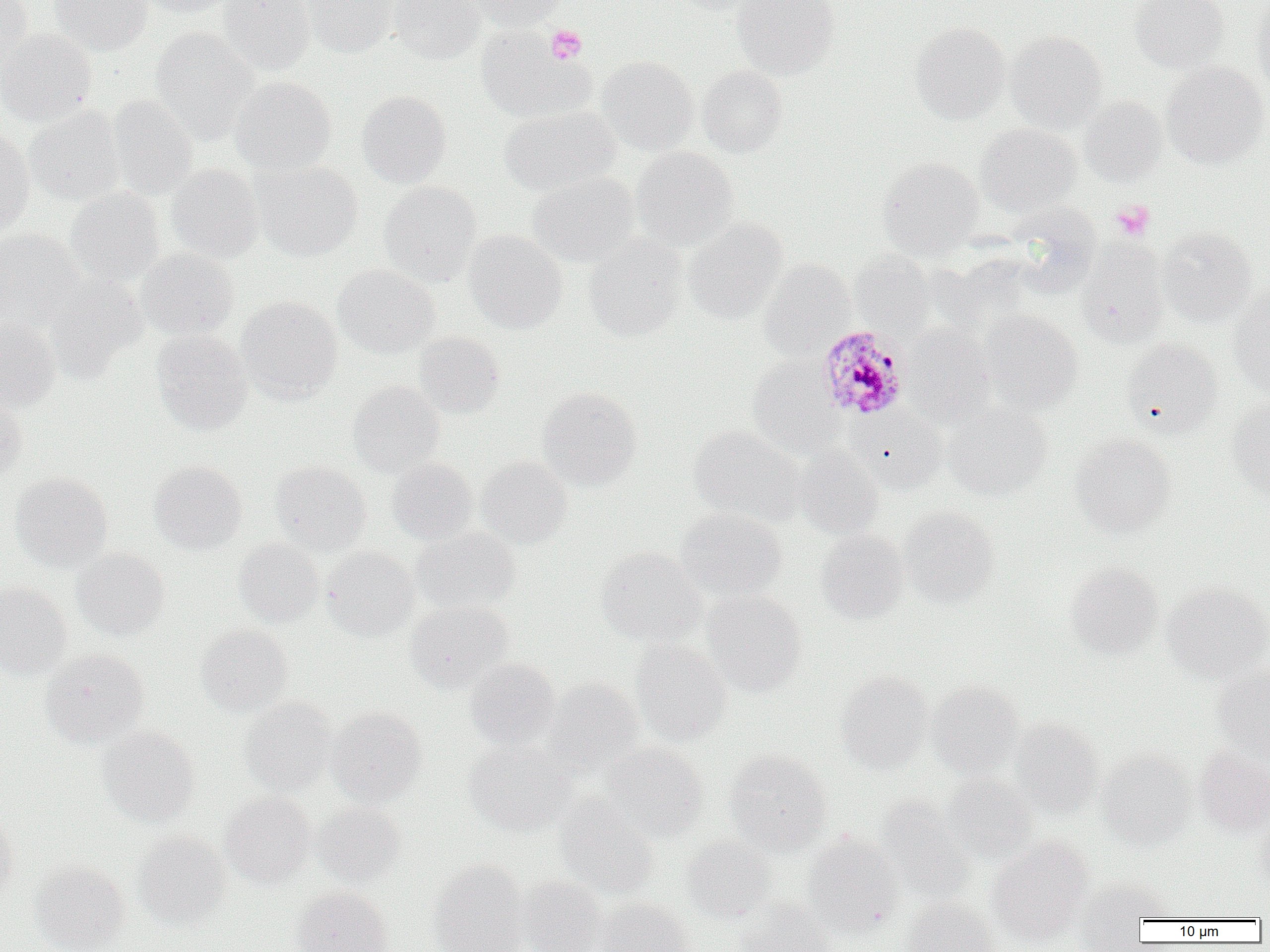
Approximate bounding boxes as (x1, y1, x2, y2) in pixels. Platelet locations: (546, 25, 586, 63), (1111, 200, 1155, 241). Uninfected red blood cell locations: (49, 0, 153, 54), (134, 0, 234, 17), (218, 0, 315, 75), (302, 0, 397, 57), (389, 0, 486, 64), (464, 0, 565, 29), (669, 0, 766, 14), (732, 0, 840, 79), (1129, 0, 1229, 73), (1249, 0, 1270, 91), (0, 1, 33, 76), (911, 22, 1011, 124), (150, 27, 258, 144), (476, 27, 593, 124), (0, 28, 96, 125), (1006, 31, 1108, 133), (596, 56, 699, 155), (1161, 63, 1269, 169), (697, 65, 788, 157), (230, 75, 336, 175), (357, 90, 451, 188), (108, 95, 198, 200), (1079, 96, 1168, 187), (498, 105, 621, 196), (24, 106, 125, 207), (975, 123, 1081, 216), (0, 127, 35, 234), (631, 146, 739, 250), (878, 157, 984, 259), (251, 160, 362, 261), (166, 164, 264, 263), (527, 172, 639, 267), (379, 181, 481, 286), (66, 186, 165, 287), (1008, 203, 1101, 295), (685, 218, 788, 323), (1157, 227, 1257, 327), (0, 229, 85, 330), (464, 230, 567, 333), (583, 235, 687, 342), (1077, 239, 1169, 347), (135, 248, 239, 339), (850, 251, 934, 336), (943, 252, 1041, 332), (759, 259, 855, 358), (333, 264, 439, 358), (45, 272, 147, 380), (1228, 289, 1270, 399), (237, 296, 341, 403), (980, 310, 1083, 413), (0, 318, 61, 411), (903, 325, 996, 426), (151, 329, 253, 435), (413, 332, 506, 418), (1121, 338, 1222, 438), (747, 356, 843, 456), (347, 380, 445, 477), (536, 387, 641, 491), (0, 389, 28, 480), (1227, 396, 1270, 498), (943, 402, 1052, 500), (849, 405, 948, 492), (688, 426, 804, 525), (1071, 433, 1175, 538), (793, 447, 883, 539), (476, 456, 572, 548), (387, 458, 478, 545), (149, 461, 247, 554), (270, 461, 371, 556), (11, 472, 112, 572), (900, 506, 998, 607), (675, 508, 786, 600), (411, 526, 521, 614), (816, 530, 909, 622), (234, 538, 324, 626), (321, 546, 419, 640), (596, 547, 706, 648), (72, 548, 170, 640), (1066, 563, 1163, 659), (1065, 570, 1268, 664), (0, 581, 71, 680), (1162, 583, 1270, 681), (702, 592, 807, 696), (405, 600, 514, 693), (196, 625, 293, 717), (631, 641, 732, 745), (41, 648, 148, 747), (465, 657, 561, 751), (1212, 666, 1270, 762), (835, 670, 933, 772), (543, 678, 644, 778), (926, 681, 1024, 777), (239, 698, 337, 796), (327, 706, 427, 805), (1011, 718, 1104, 816), (98, 726, 199, 826), (464, 741, 577, 835), (601, 742, 708, 841), (1194, 746, 1270, 836), (725, 751, 831, 854), (1097, 751, 1196, 848), (942, 774, 1039, 863), (220, 792, 316, 887), (555, 797, 660, 898), (874, 797, 974, 903), (313, 802, 406, 888), (0, 808, 17, 899), (1252, 815, 1270, 892), (133, 831, 230, 930), (802, 834, 903, 937), (681, 835, 776, 923), (988, 837, 1092, 944), (31, 860, 130, 952), (430, 861, 529, 952), (517, 877, 607, 952), (1072, 879, 1166, 948), (291, 886, 392, 952), (733, 897, 836, 952), (595, 898, 696, 952), (901, 898, 999, 952). Plasmodium malariae-infected red blood cell locations: (816, 326, 911, 420). Slide-level diagnosis: Plasmodium malariae. Image is 1270×952 pixels. Light microscopy. Captured at 1000x magnification. Thin blood film. Single field of view.